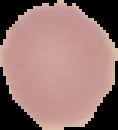
{
  "image_type": "cell region segmented out of the field of view; surrounding area masked to black",
  "result": "no Plasmodium parasites seen",
  "preparation": "thin blood film",
  "image_size": "118×130 pixels"
}